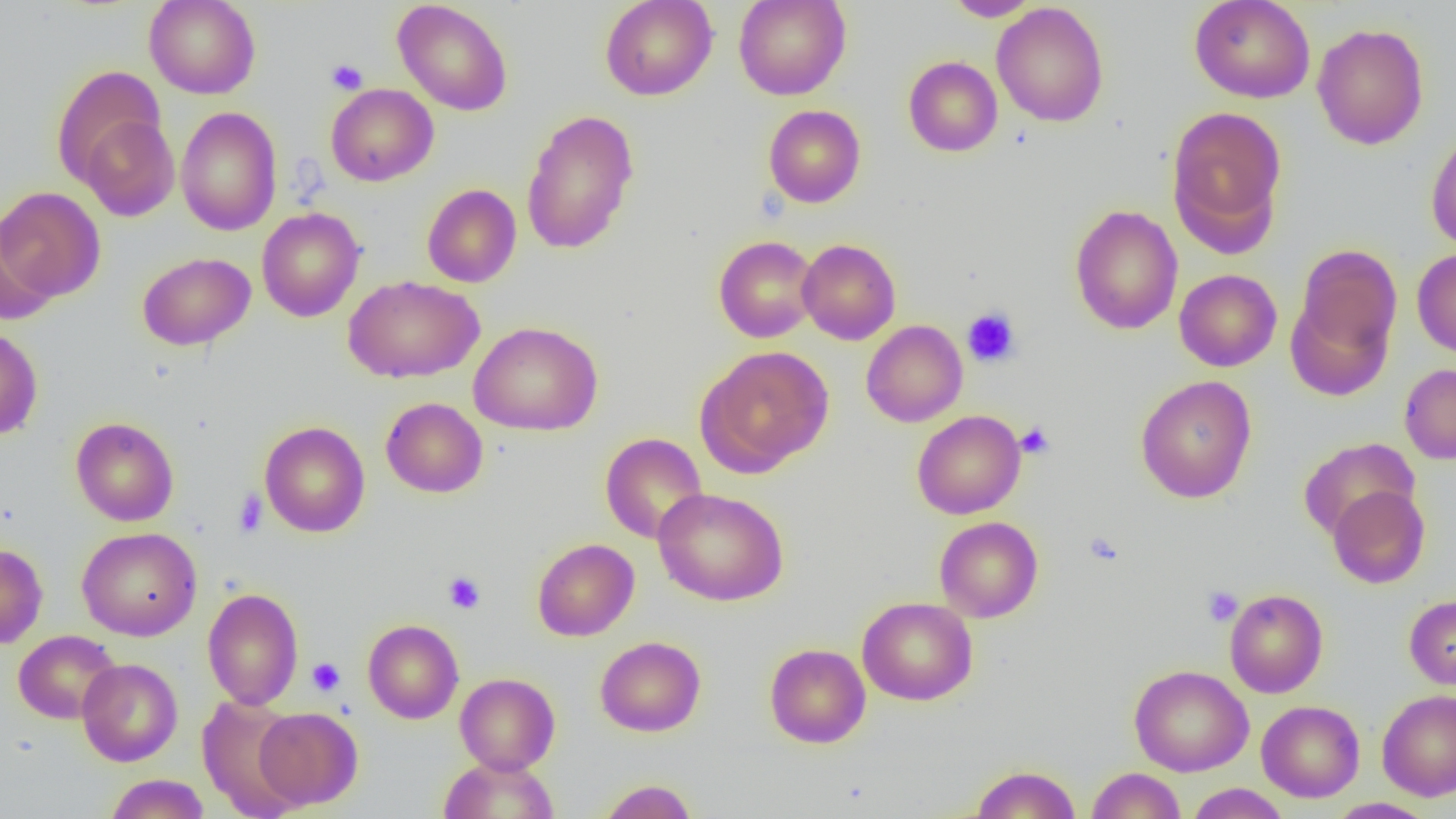
Summary:
  - Coordinate format: approximate bounding boxes as (x1,y1)-(x2,y2) corner pairs in pixels
  - Platelet locations: (326,59)-(368,95), (962,307)-(1021,368), (1016,422)-(1055,459), (233,489)-(268,538), (1083,531)-(1124,566), (443,571)-(486,614), (1202,586)-(1243,626), (307,657)-(345,696)
  - Uninfected red blood cell locations: (144,0)-(261,99), (393,0)-(513,116), (600,0)-(718,101), (733,0)-(852,100), (1189,0)-(1315,103), (945,1)-(1040,21), (991,2)-(1109,127), (1312,23)-(1429,150), (903,56)-(1003,157), (51,65)-(169,192), (325,83)-(439,187), (763,104)-(865,208), (175,105)-(282,236), (1166,105)-(1287,253), (521,109)-(640,255), (75,111)-(180,220), (1425,130)-(1456,252), (422,183)-(521,288), (0,186)-(106,303), (1069,204)-(1183,334), (256,207)-(365,322), (0,218)-(59,323), (713,235)-(820,343), (797,239)-(901,345), (1292,244)-(1402,370), (1412,248)-(1456,358), (137,252)-(255,351), (1174,269)-(1282,371), (344,276)-(484,383), (1285,294)-(1396,401), (861,320)-(968,427), (469,321)-(603,436), (0,326)-(43,440), (695,346)-(834,476), (1399,363)-(1456,464), (1135,376)-(1257,503), (381,397)-(488,498), (912,410)-(1026,519), (70,417)-(179,526), (259,421)-(370,537), (600,432)-(708,544), (1298,437)-(1420,541), (1327,485)-(1430,589), (652,487)-(789,606), (934,516)-(1043,622), (77,527)-(202,641), (532,538)-(639,641), (0,543)-(48,649), (203,587)-(303,710), (1224,589)-(1328,698), (1404,594)-(1456,689), (857,597)-(978,705), (362,619)-(464,724), (13,630)-(122,724), (595,636)-(706,737), (765,643)-(871,748), (77,658)-(182,766), (1129,664)-(1253,776), (455,673)-(560,774), (1376,688)-(1456,802), (197,695)-(307,819), (1256,700)-(1364,802), (254,707)-(363,810), (438,756)-(560,818), (970,764)-(1081,818), (1086,767)-(1186,819), (105,773)-(210,818), (597,779)-(697,819), (1185,784)-(1291,818), (1327,798)-(1437,819)
  - Slide-level diagnosis: negative for blood parasites
  - Magnification: 1000x
  - Field of view: one of a larger specimen
  - Modality: light microscopy
  - Preparation: thin blood film
  - Image size: 1456×819 pixels